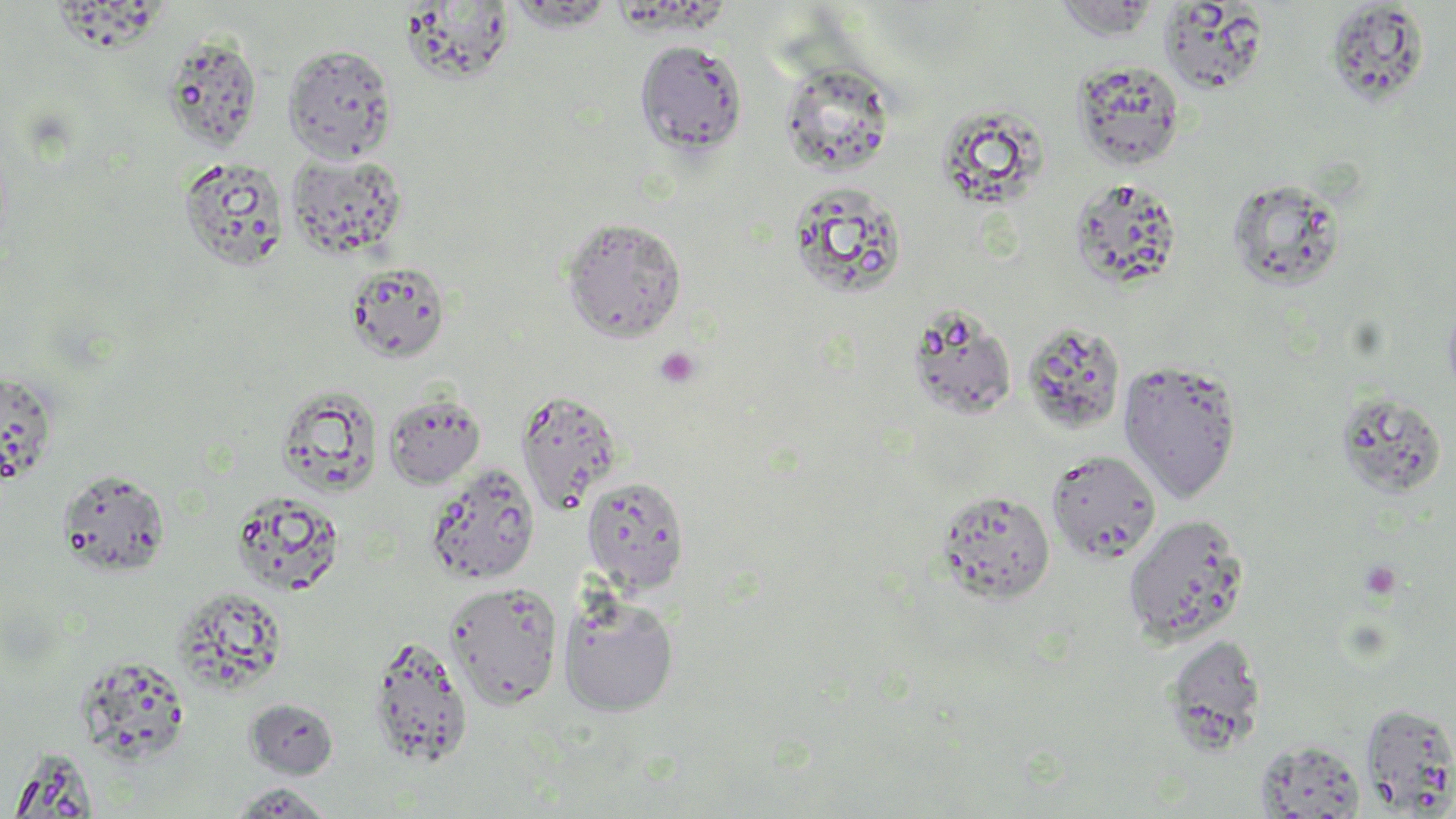

slide_level_diagnosis: no evidence of blood parasites
image_size: 1456×819 pixels
stain: May-Grünwald-Giemsa
magnification: 1000x
uninfected_red_blood_cell_locations: 'approximate bounding boxes as named x1/y1/x2/y2 corners in pixels: (x1=1052, y1=0, x2=1163, y2=40), (x1=1324, y1=1, x2=1431, y2=110), (x1=1158, y1=2, x2=1270, y2=94), (x1=400, y1=4, x2=518, y2=84), (x1=160, y1=33, x2=264, y2=152), (x1=635, y1=39, x2=748, y2=157), (x1=282, y1=44, x2=397, y2=163), (x1=1071, y1=59, x2=1185, y2=171), (x1=780, y1=64, x2=897, y2=176), (x1=937, y1=104, x2=1055, y2=204), (x1=286, y1=151, x2=409, y2=261), (x1=178, y1=156, x2=290, y2=273), (x1=1068, y1=177, x2=1184, y2=291), (x1=1226, y1=177, x2=1348, y2=292), (x1=787, y1=182, x2=909, y2=301), (x1=561, y1=217, x2=687, y2=342), (x1=344, y1=262, x2=451, y2=362), (x1=906, y1=303, x2=1018, y2=421), (x1=1021, y1=322, x2=1127, y2=435), (x1=1118, y1=358, x2=1243, y2=503), (x1=0, y1=371, x2=58, y2=484), (x1=277, y1=387, x2=381, y2=495), (x1=515, y1=389, x2=623, y2=516), (x1=1334, y1=390, x2=1448, y2=499), (x1=383, y1=392, x2=486, y2=490), (x1=1045, y1=450, x2=1161, y2=564), (x1=424, y1=462, x2=541, y2=585), (x1=57, y1=469, x2=172, y2=577), (x1=581, y1=476, x2=690, y2=594), (x1=935, y1=489, x2=1057, y2=605), (x1=229, y1=494, x2=350, y2=600), (x1=1123, y1=514, x2=1250, y2=646), (x1=444, y1=581, x2=563, y2=710), (x1=170, y1=586, x2=291, y2=694), (x1=558, y1=592, x2=679, y2=717), (x1=1163, y1=633, x2=1268, y2=756), (x1=367, y1=634, x2=473, y2=768), (x1=245, y1=698, x2=340, y2=778), (x1=1360, y1=702, x2=1456, y2=815), (x1=1254, y1=740, x2=1366, y2=818), (x1=7, y1=747, x2=99, y2=818), (x1=229, y1=782, x2=336, y2=817)'
preparation: thin blood smear
field_of_view: single
modality: light microscopy
platelet_locations: 'approximate bounding boxes as named x1/y1/x2/y2 corners in pixels: (x1=655, y1=346, x2=700, y2=389), (x1=1359, y1=560, x2=1402, y2=600)'